Name the blood parasite species.
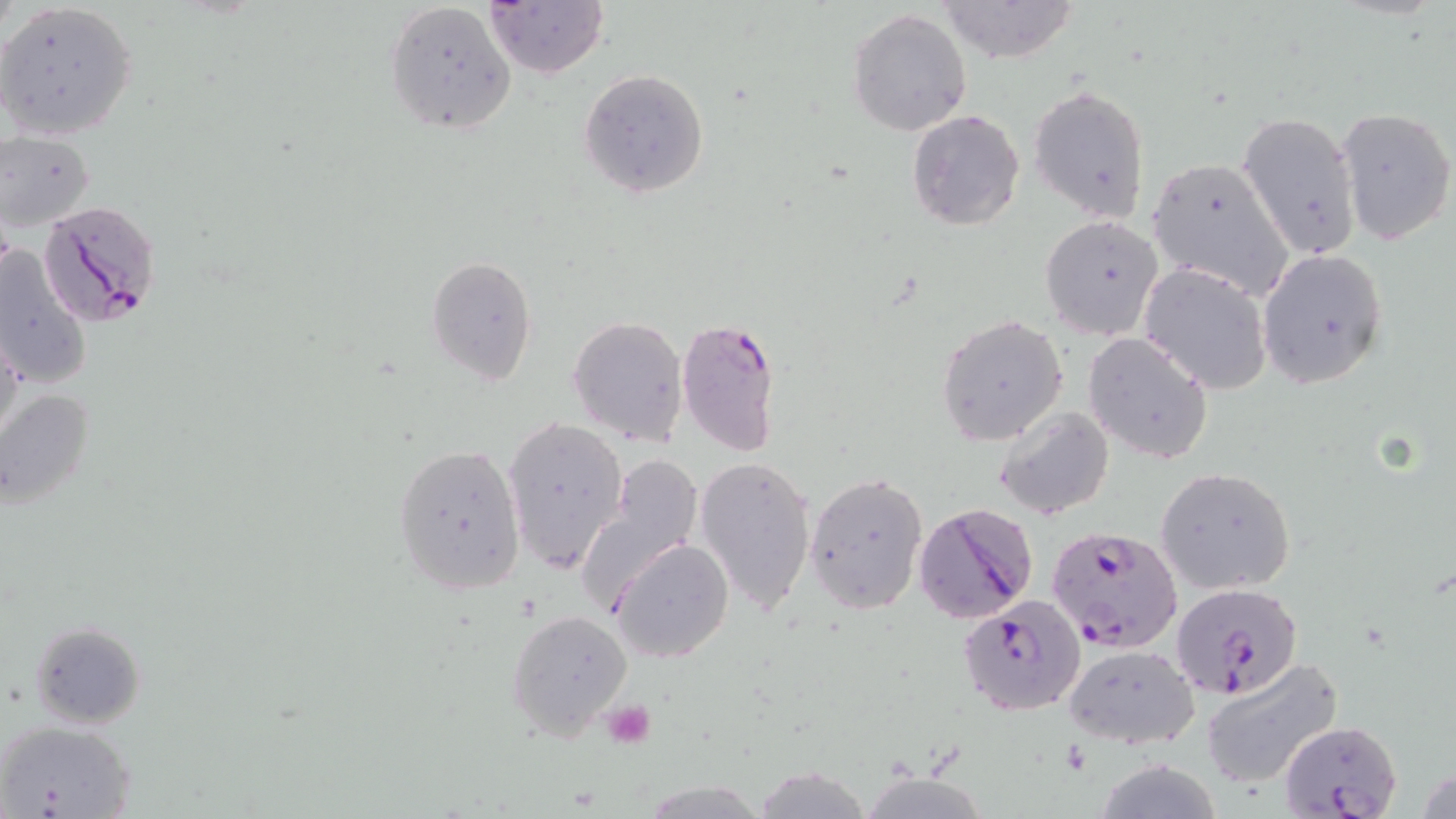
Plasmodium falciparum.

Summary:
  - Coordinate format: approximate bounding boxes as [x1, y1, x2, y2] in pixels
  - Platelet locations: [601, 701, 656, 748]
  - Uninfected red blood cell locations: [484, 0, 607, 78], [939, 0, 1082, 66], [384, 1, 517, 136], [0, 2, 139, 140], [848, 8, 972, 137], [578, 68, 709, 198], [1030, 87, 1151, 222], [1334, 105, 1455, 248], [907, 109, 1025, 230], [1235, 111, 1362, 259], [1, 130, 97, 230], [1147, 156, 1295, 299], [1039, 215, 1162, 340], [0, 244, 91, 391], [1257, 249, 1389, 387], [425, 255, 538, 387], [1140, 262, 1272, 393], [937, 314, 1068, 447], [568, 315, 689, 446], [0, 324, 24, 453], [1084, 331, 1214, 464], [0, 388, 96, 511], [994, 405, 1115, 520], [503, 415, 627, 572], [393, 442, 526, 597], [580, 453, 704, 608], [694, 454, 818, 615], [1155, 467, 1295, 595], [805, 471, 928, 614], [610, 536, 733, 663], [506, 608, 633, 739], [29, 620, 146, 730], [1064, 643, 1199, 748], [1200, 656, 1344, 790], [0, 720, 135, 818], [749, 765, 877, 819]
  - Plasmodium falciparum-infected red blood cell locations: [37, 200, 162, 328], [676, 315, 782, 458], [913, 502, 1039, 623], [1047, 524, 1183, 653], [1169, 581, 1307, 708], [959, 595, 1085, 716], [1277, 720, 1401, 818]
  - Preparation: thin blood film
  - Stain: May-Grünwald-Giemsa
  - Field of view: one of a larger specimen
  - Image size: 1456×819 pixels
  - Magnification: 1000x
  - Modality: light microscopy